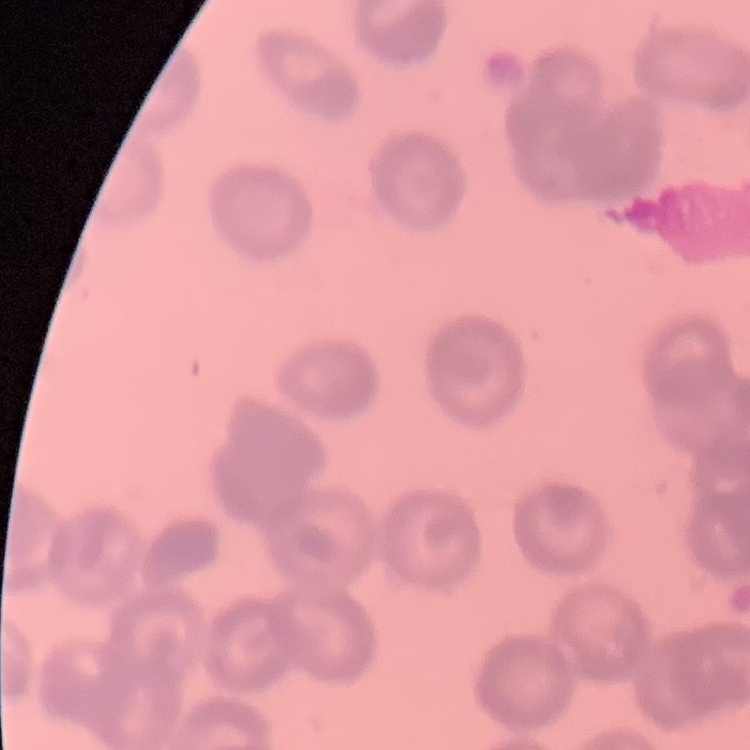

Summary:
  - Erythrocyte morphology: rouleaux formation
  - Stain: Field's or Giemsa
  - Preparation: thin peripheral smear
  - Image type: one tile cut from a larger photomicrograph